Point out each malaria parasite.
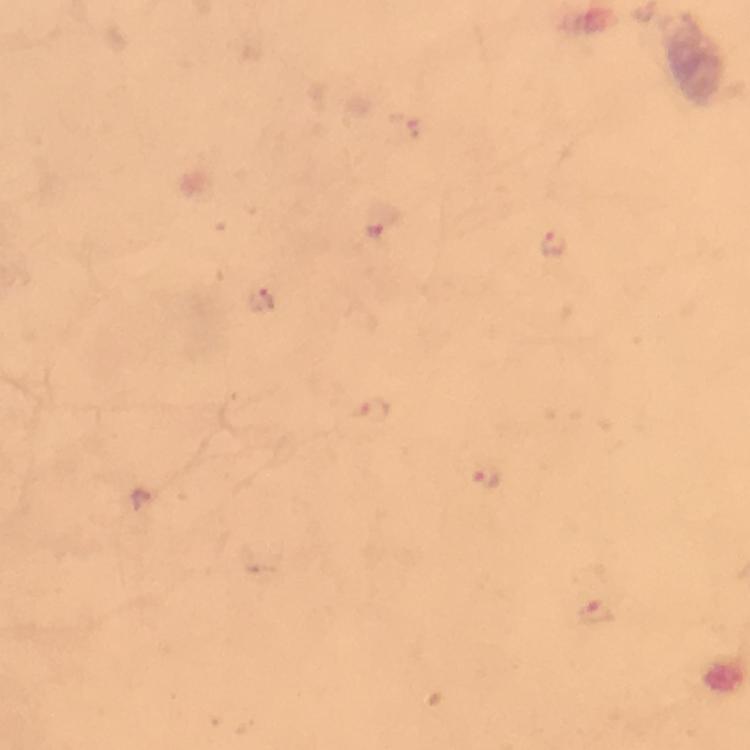

Approximate centers as (x, y) in pixels.
Malaria parasites: (402, 132), (379, 219), (554, 244), (259, 300), (371, 409), (486, 473), (141, 498), (595, 611).

{
  "stain": "Giemsa",
  "capture": "smartphone mounted on the microscope",
  "cropped_from": "a single field of view",
  "context": "from a diagnostic examination for malaria",
  "image_size": "750×750 pixels",
  "preparation": "thick blood film",
  "magnification": "100x",
  "immersion_oil": "used"
}